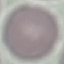
{
  "malaria_status": "uninfected",
  "preparation": "thin blood film",
  "image_type": "automatically extracted cell patch, resized to 64 × 64 pixels",
  "capture": "smartphone camera at the microscope eyepiece",
  "stain": "Giemsa"
}